Outline each Plasmodium vivax-infected red blood cell.
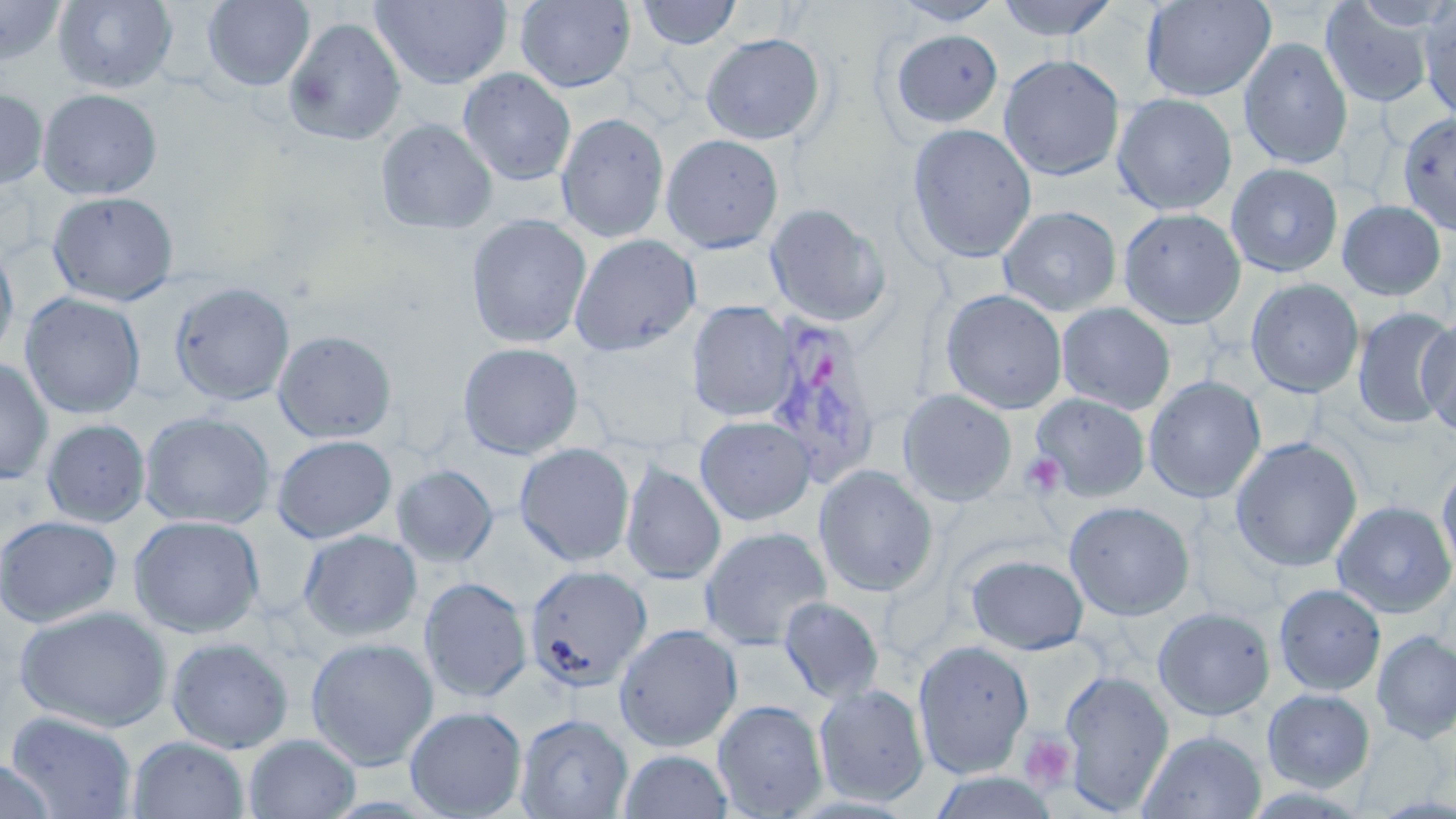
Approximate bounding boxes as [x1, y1, x2, y2] in pixels.
Plasmodium vivax-infected red blood cells: [761, 312, 884, 486].

slide-level diagnosis = Plasmodium vivax
magnification = 1000x
preparation = thin blood film
stain = May-Grünwald-Giemsa
platelet locations = approximate bounding boxes as [x1, y1, x2, y2] in pixels: [1020, 451, 1066, 498], [1019, 734, 1076, 791]
uninfected red blood cell locations = approximate bounding boxes as [x1, y1, x2, y2] in pixels: [52, 0, 178, 93], [202, 0, 315, 91], [515, 0, 636, 92], [635, 0, 743, 49], [890, 0, 1006, 26], [995, 0, 1119, 41], [1141, 0, 1275, 102], [0, 1, 67, 68], [371, 1, 512, 89], [1321, 1, 1435, 109], [1419, 4, 1456, 122], [283, 17, 407, 146], [888, 28, 1004, 129], [701, 33, 826, 145], [1239, 37, 1353, 170], [998, 54, 1124, 181], [458, 68, 576, 186], [0, 88, 48, 190], [37, 88, 163, 200], [1112, 94, 1237, 215], [1398, 111, 1456, 237], [556, 113, 670, 243], [375, 118, 498, 234], [906, 123, 1037, 264], [661, 133, 784, 254], [1226, 163, 1343, 277], [47, 191, 179, 306], [1337, 200, 1446, 301], [765, 203, 891, 326], [998, 205, 1121, 316], [1118, 207, 1246, 329], [465, 214, 591, 349], [569, 234, 702, 356], [684, 238, 786, 316], [0, 241, 19, 366], [1245, 278, 1365, 398], [169, 281, 295, 406], [939, 289, 1068, 414], [20, 292, 145, 419], [687, 301, 796, 422], [1056, 302, 1176, 414], [1352, 307, 1455, 429], [1419, 317, 1456, 436], [273, 330, 397, 444], [458, 341, 584, 459], [0, 357, 53, 484], [1143, 375, 1266, 503], [898, 389, 1017, 507], [1031, 393, 1150, 500], [139, 411, 275, 529], [695, 416, 815, 525], [41, 419, 150, 527], [272, 434, 397, 543], [1229, 437, 1363, 573], [514, 443, 635, 566], [1436, 459, 1456, 580], [621, 461, 726, 585], [392, 465, 498, 567], [813, 465, 939, 597], [1332, 500, 1456, 619], [1064, 501, 1195, 621], [0, 514, 121, 628], [128, 515, 265, 638], [699, 526, 832, 650], [298, 529, 422, 642], [966, 554, 1089, 655], [524, 564, 653, 692], [419, 577, 532, 703], [1274, 583, 1386, 695], [778, 596, 884, 704], [15, 604, 174, 732], [1153, 607, 1275, 720], [614, 623, 743, 751], [1372, 631, 1456, 743], [166, 636, 294, 754], [306, 637, 439, 770], [912, 639, 1034, 778], [1059, 669, 1173, 814], [814, 683, 929, 806], [1262, 688, 1375, 792], [713, 699, 828, 818], [404, 706, 527, 818], [5, 711, 138, 819], [516, 713, 633, 818], [1139, 729, 1265, 819], [243, 734, 360, 818], [127, 736, 250, 819], [619, 749, 732, 818], [0, 759, 57, 819], [930, 771, 1060, 818]
modality = light microscopy
field of view = one of a larger specimen
image size = 1456×819 pixels